Name the cell type shown.
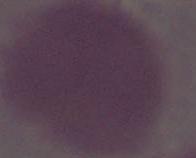

An erythrocyte.

{
  "magnification": "1000x",
  "modality": "photomicrograph"
}